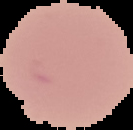
preparation = thin blood film
image size = 133×130 pixels
malaria status = uninfected
image type = segmented cell region with the area outside set to black